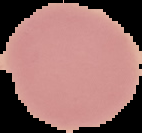

image_type: segmented cell region with the area outside set to black
preparation: thin blood film
image_size: 142×133 pixels
result: no malaria parasites seen